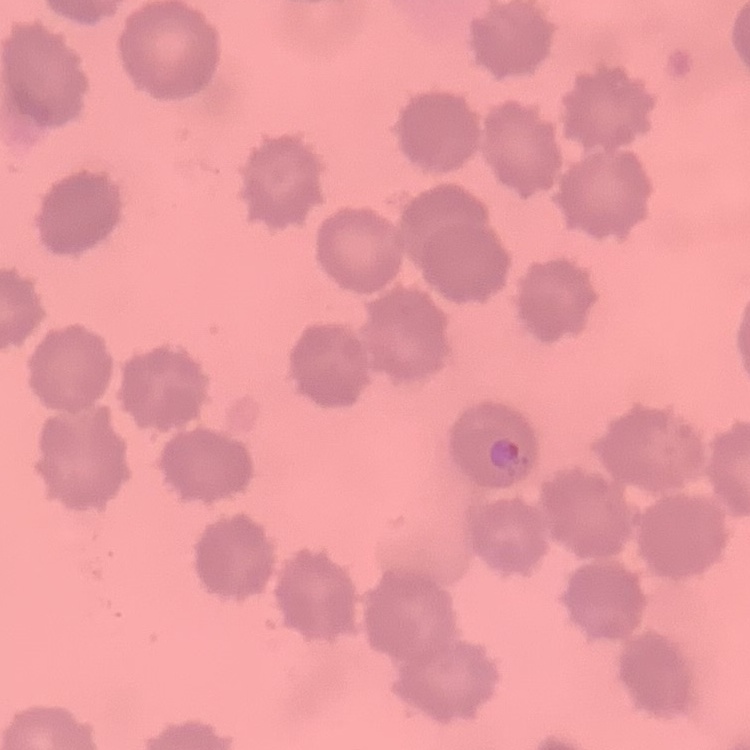

The red blood cells show no rouleaux formation. Stained with either Field's or Giemsa. Thin peripheral smear. One tile cut from a larger photomicrograph.